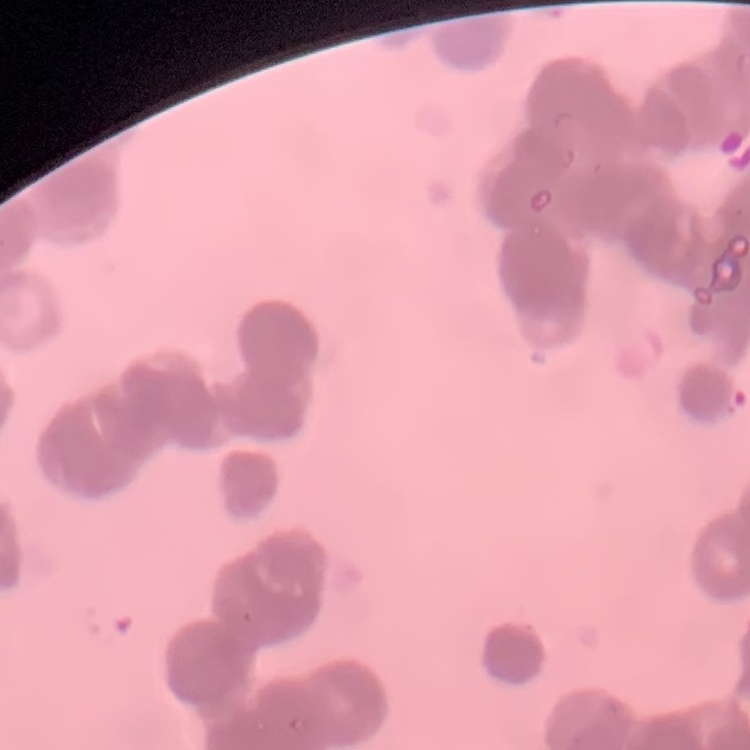

{
  "red_blood_cell_morphology": "rouleaux formation",
  "preparation": "thin blood smear",
  "image_type": "one tile cut from a larger photomicrograph",
  "stain": "Field's or Giemsa"
}